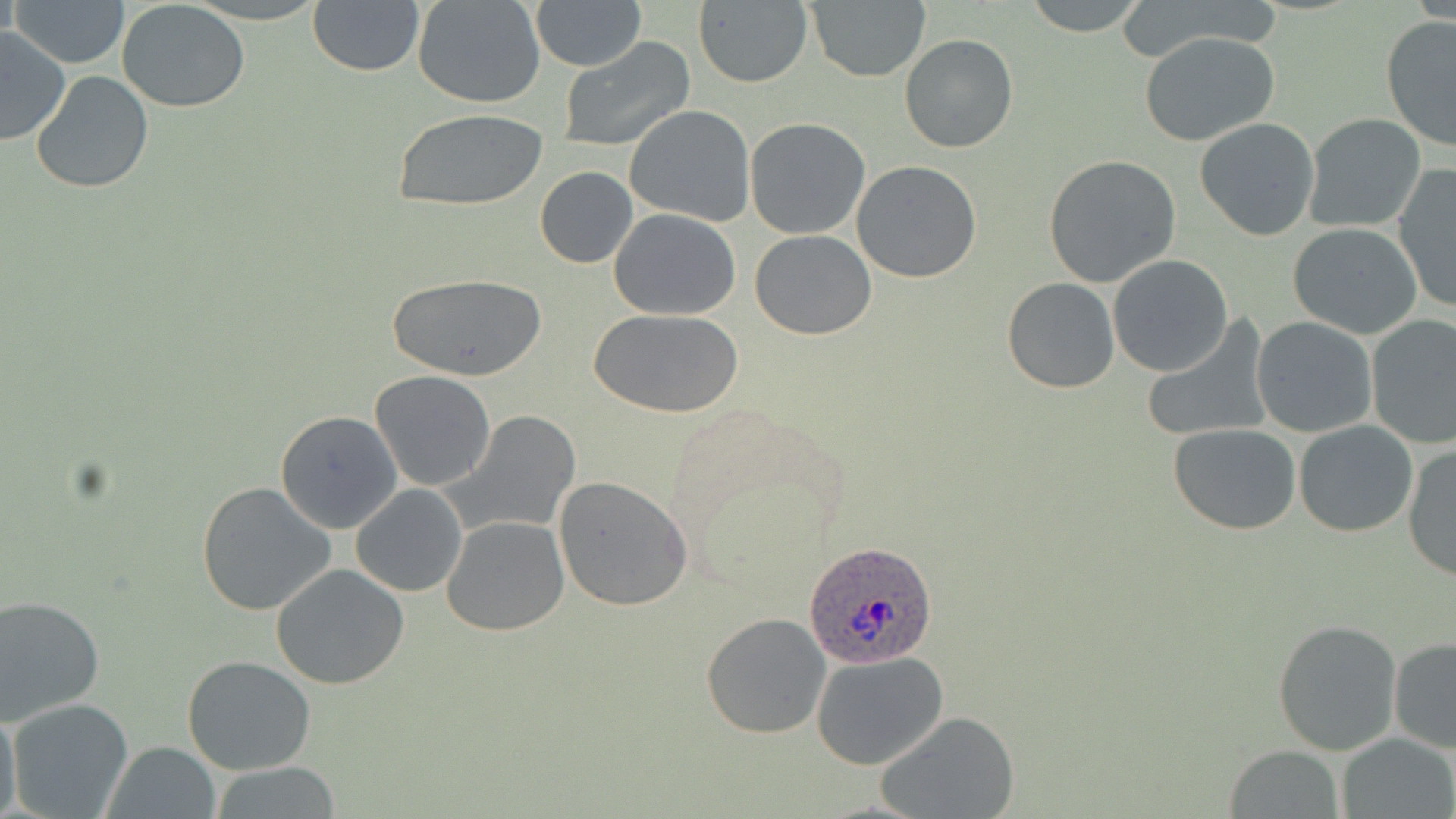
Summary:
  - Coordinate format: approximate bounding boxes as (x1, y1, x2, y2) in pixels
  - Uninfected red blood cell locations: (9, 0, 129, 69), (307, 0, 425, 76), (411, 0, 548, 108), (530, 0, 645, 71), (692, 0, 813, 87), (805, 0, 929, 82), (1020, 0, 1149, 34), (117, 2, 251, 113), (1380, 17, 1456, 153), (0, 27, 73, 146), (1139, 31, 1279, 147), (900, 32, 1018, 153), (559, 36, 695, 152), (31, 70, 154, 194), (624, 104, 756, 226), (390, 107, 550, 212), (1304, 113, 1426, 233), (1195, 117, 1322, 240), (744, 118, 871, 239), (1044, 154, 1183, 289), (851, 161, 983, 283), (1392, 165, 1456, 314), (536, 167, 638, 267), (608, 208, 740, 320), (1286, 222, 1424, 337), (750, 231, 877, 340), (1107, 255, 1235, 375), (388, 272, 546, 384), (1002, 277, 1121, 393), (593, 309, 740, 418), (1140, 314, 1274, 444), (1251, 316, 1378, 438), (1366, 316, 1456, 449), (369, 371, 497, 492), (274, 410, 402, 532), (452, 411, 580, 535), (1293, 420, 1419, 536), (1168, 423, 1301, 534), (1402, 442, 1456, 582), (553, 476, 695, 612), (195, 481, 337, 617), (351, 485, 467, 598), (441, 516, 569, 636), (271, 564, 410, 690), (0, 596, 104, 724), (701, 611, 830, 739), (1272, 620, 1403, 755), (1388, 637, 1456, 755), (812, 652, 949, 769), (182, 653, 317, 774), (5, 697, 135, 819), (0, 701, 23, 819), (876, 709, 1020, 819), (1337, 733, 1455, 819), (104, 741, 221, 819), (1225, 745, 1345, 818), (205, 763, 345, 818)
  - Plasmodium ovale-infected red blood cell locations: (801, 543, 940, 668)
  - Slide-level diagnosis: Plasmodium ovale
  - Stain: May-Grünwald-Giemsa
  - Field of view: single
  - Magnification: 1000x
  - Modality: light microscopy
  - Image size: 1456×819 pixels
  - Preparation: thin blood smear